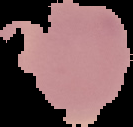
Image is 133×127 pixels. Cell region segmented out of the field of view; the surrounding area is masked to black. Result: no Plasmodium parasites detected. From a thin blood film.